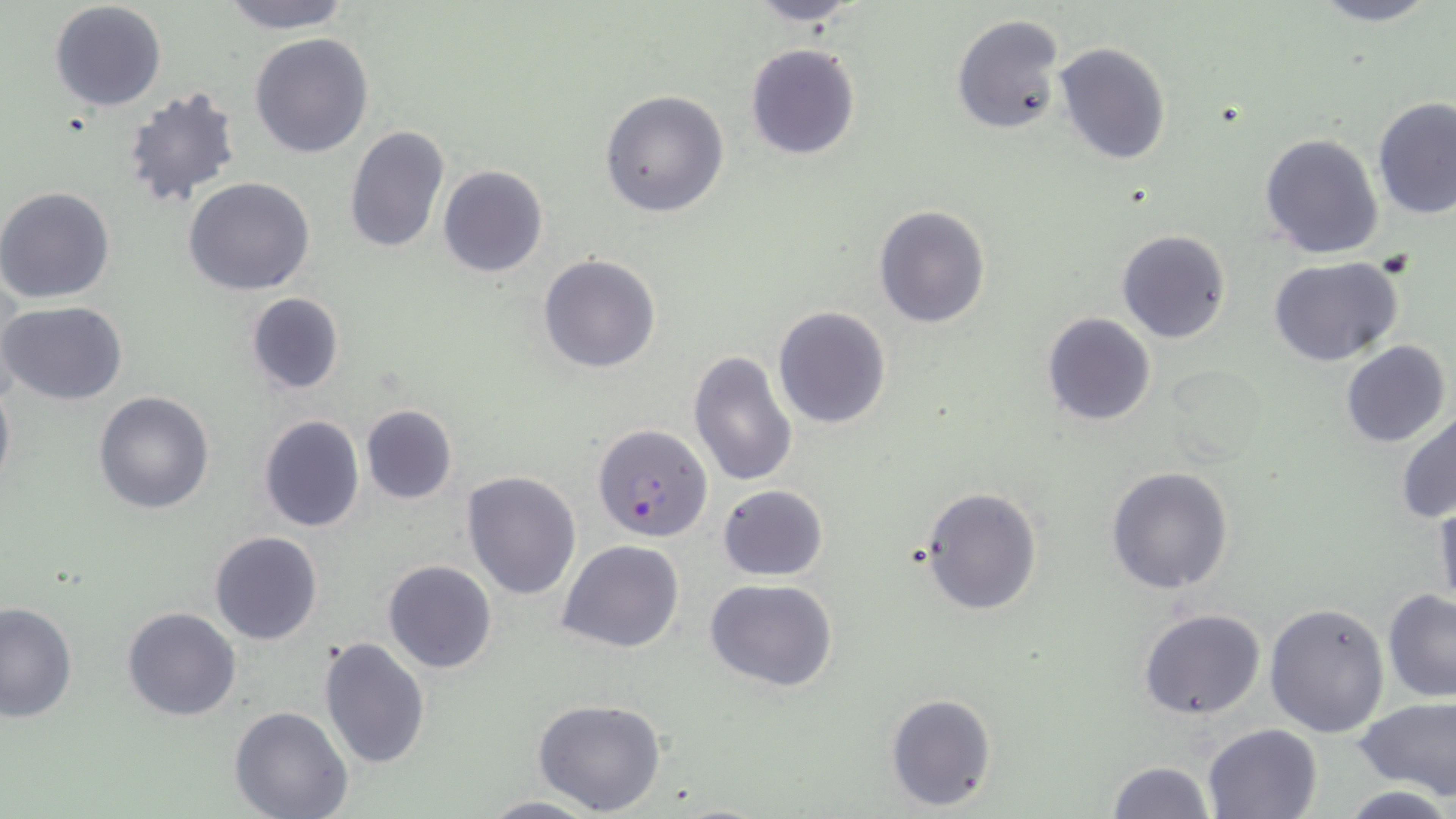 Approximate bounding boxes as [x1, y1, x2, y2] in pixels. Uninfected red blood cell locations: [217, 0, 354, 31], [1302, 0, 1447, 27], [745, 1, 868, 27], [48, 2, 167, 113], [950, 14, 1065, 136], [250, 32, 375, 159], [744, 42, 861, 160], [1054, 42, 1172, 166], [119, 83, 242, 210], [600, 89, 730, 217], [1373, 99, 1456, 222], [344, 124, 450, 255], [1259, 133, 1385, 260], [438, 165, 550, 278], [184, 177, 315, 296], [0, 186, 116, 305], [873, 205, 990, 330], [1117, 230, 1231, 344], [538, 253, 662, 374], [1266, 255, 1404, 367], [245, 292, 345, 396], [0, 301, 129, 404], [772, 305, 891, 431], [1042, 313, 1156, 426], [1340, 341, 1450, 448], [687, 349, 798, 488], [1167, 363, 1272, 468], [0, 377, 15, 497], [93, 390, 216, 514], [360, 403, 457, 505], [1396, 409, 1456, 524], [257, 414, 365, 533], [1106, 465, 1234, 595], [462, 470, 581, 598], [717, 485, 829, 581], [917, 485, 1043, 616], [1431, 497, 1455, 615], [209, 530, 324, 645], [559, 539, 684, 653], [383, 559, 497, 673], [705, 577, 840, 692], [1382, 589, 1456, 702], [0, 601, 77, 723], [1264, 601, 1391, 739], [121, 606, 243, 721], [1138, 606, 1267, 720], [318, 636, 431, 772], [885, 692, 997, 812], [1356, 696, 1456, 798], [533, 698, 666, 816], [230, 707, 352, 819], [1203, 722, 1322, 817], [1107, 760, 1214, 818], [1341, 785, 1452, 817], [480, 794, 601, 818]. Plasmodium falciparum-infected red blood cell locations: [591, 423, 715, 544]. Slide-level diagnosis: Plasmodium falciparum. Optical microscopy. 1000x magnification. Image is 1456×819 pixels. Thin blood smear. May-Grünwald-Giemsa stain. Single field of view.